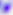
magnification = 400x
modality = micrograph
identification = Toxoplasma gondii